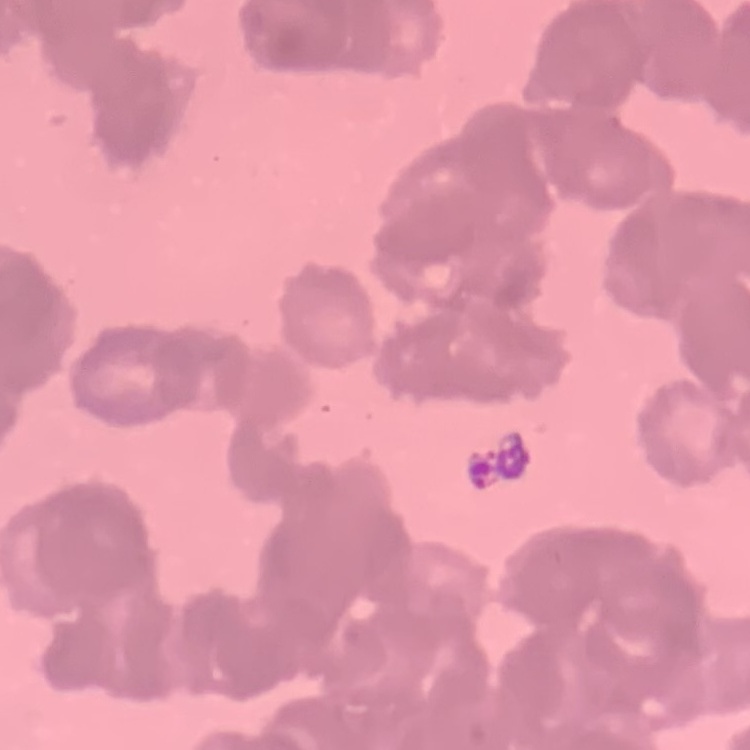

The red blood cells show rouleaux formation. Square crop of a larger photomicrograph. Stained with either Field's or Giemsa. Thin blood film.